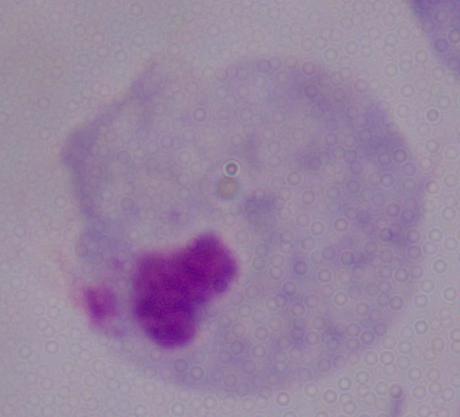

Summary:
  - Magnification: 1000x
  - Identification: trichomonad
  - Modality: photomicrograph